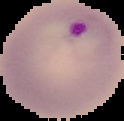

Summary:
  - Result: Plasmodium parasites detected
  - Image size: 124×121 pixels
  - Preparation: thin blood smear
  - Image type: segmented cell region on a black background